Locate every Plasmodium falciparum-infected red blood cell.
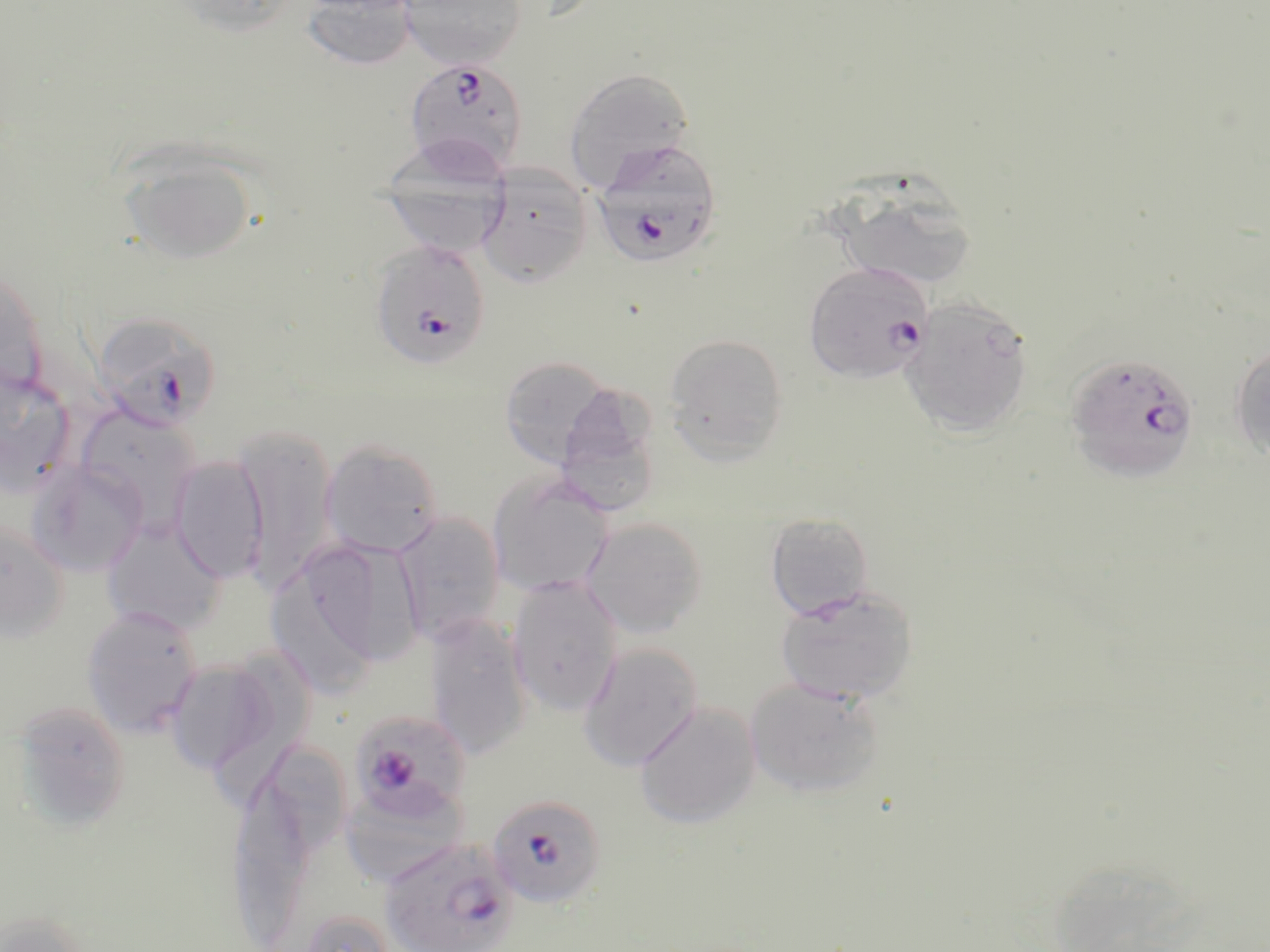
Approximate bounding boxes as named x1/y1/x2/y2 corners in pixels.
Plasmodium falciparum-infected red blood cells: (x1=403, y1=58, x2=530, y2=177), (x1=591, y1=138, x2=723, y2=269), (x1=368, y1=239, x2=491, y2=370), (x1=804, y1=261, x2=933, y2=383), (x1=92, y1=311, x2=224, y2=432), (x1=1065, y1=352, x2=1199, y2=484), (x1=348, y1=711, x2=474, y2=825), (x1=487, y1=793, x2=608, y2=910), (x1=380, y1=837, x2=519, y2=952).

Uninfected red blood cell locations: (x1=168, y1=0, x2=300, y2=36), (x1=399, y1=0, x2=527, y2=69), (x1=301, y1=1, x2=419, y2=71), (x1=564, y1=68, x2=695, y2=189), (x1=117, y1=147, x2=258, y2=266), (x1=477, y1=166, x2=594, y2=287), (x1=379, y1=167, x2=511, y2=259), (x1=827, y1=178, x2=981, y2=292), (x1=0, y1=261, x2=49, y2=398), (x1=899, y1=296, x2=1034, y2=438), (x1=663, y1=333, x2=789, y2=463), (x1=1229, y1=343, x2=1270, y2=462), (x1=498, y1=355, x2=618, y2=470), (x1=0, y1=363, x2=79, y2=498), (x1=555, y1=381, x2=667, y2=512), (x1=75, y1=404, x2=202, y2=530), (x1=235, y1=422, x2=337, y2=591), (x1=319, y1=439, x2=445, y2=559), (x1=168, y1=454, x2=269, y2=583), (x1=26, y1=461, x2=148, y2=576), (x1=486, y1=469, x2=614, y2=596), (x1=394, y1=511, x2=505, y2=645), (x1=765, y1=513, x2=875, y2=618), (x1=581, y1=516, x2=709, y2=638), (x1=101, y1=518, x2=228, y2=635), (x1=0, y1=519, x2=70, y2=641), (x1=275, y1=532, x2=423, y2=678), (x1=506, y1=573, x2=624, y2=716), (x1=775, y1=584, x2=918, y2=705), (x1=80, y1=606, x2=203, y2=737), (x1=424, y1=614, x2=532, y2=760), (x1=577, y1=642, x2=704, y2=771), (x1=202, y1=647, x2=317, y2=810), (x1=164, y1=658, x2=281, y2=775), (x1=744, y1=676, x2=885, y2=798), (x1=11, y1=700, x2=132, y2=832), (x1=634, y1=700, x2=761, y2=829), (x1=263, y1=741, x2=351, y2=858), (x1=232, y1=778, x2=317, y2=944), (x1=342, y1=786, x2=468, y2=883), (x1=293, y1=907, x2=396, y2=952), (x1=0, y1=909, x2=96, y2=952). Slide-level diagnosis: Plasmodium falciparum. Captured at 1000x magnification. One field of a larger specimen. Thin blood smear. Light microscopy. Image is 1270×952 pixels. May-Grünwald-Giemsa-stained preparation.